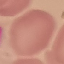
Result: no malaria parasites seen. Giemsa stain. Cell patch, automatically extracted from a larger field of view and resized to 64 × 64 pixels. Photographed with a smartphone camera at the microscope eyepiece. Thin smear of blood.